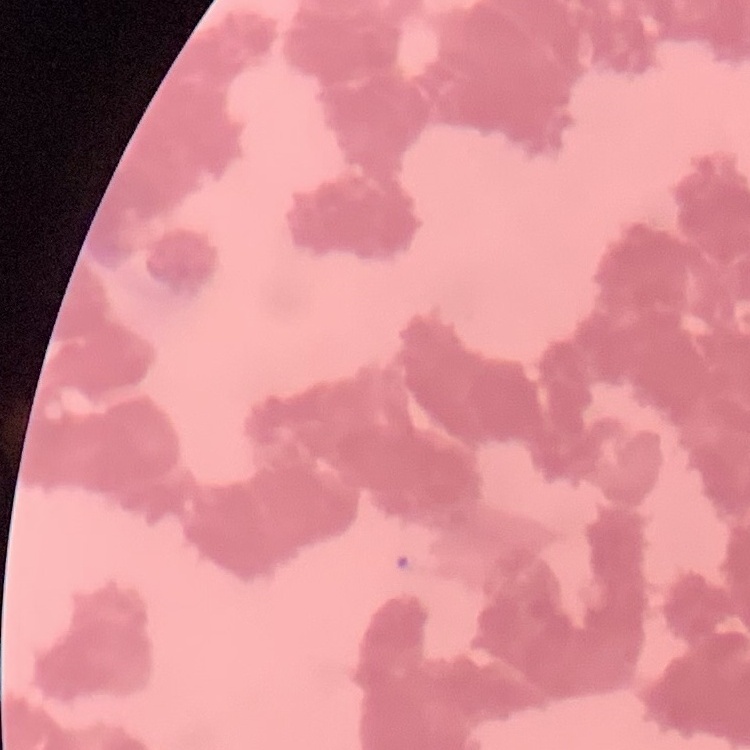
The erythrocytes exhibit rouleaux formation. Field's or Giemsa stain. One tile cut from a larger photomicrograph. Thin blood film.